Give the position of every Plasmodium parasite.
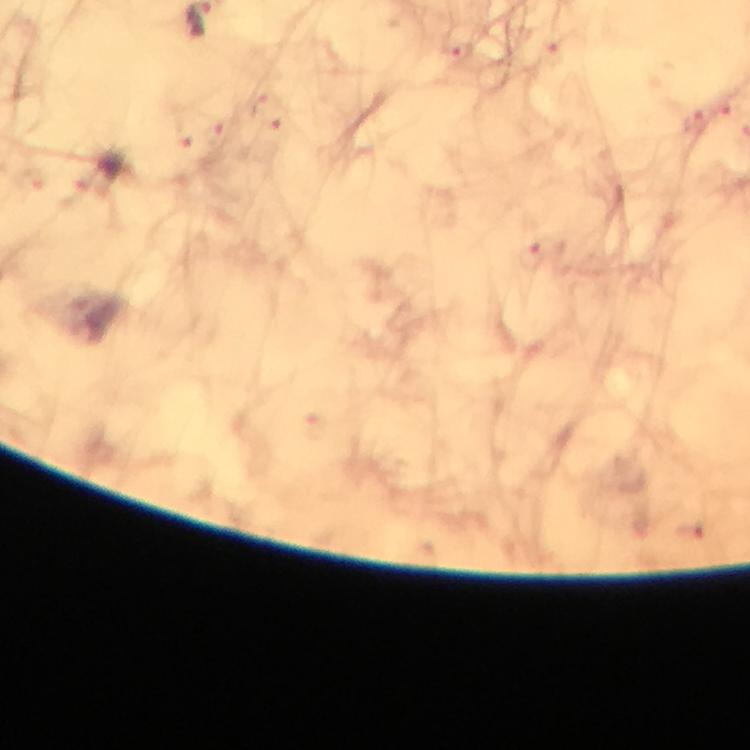
Approximate object centers, in pixels from the top-left corner.
Plasmodium parasites: (x=458, y=51), (x=257, y=105), (x=724, y=112), (x=696, y=123), (x=277, y=128), (x=218, y=133), (x=184, y=136), (x=530, y=255).

stain = Giemsa
immersion oil = used
magnification = 100x
image size = 750×750 pixels
preparation = thick smear
cropped from = a single field of view
context = from a diagnostic examination for malaria
capture = smartphone camera through the microscope